Report the malaria status.
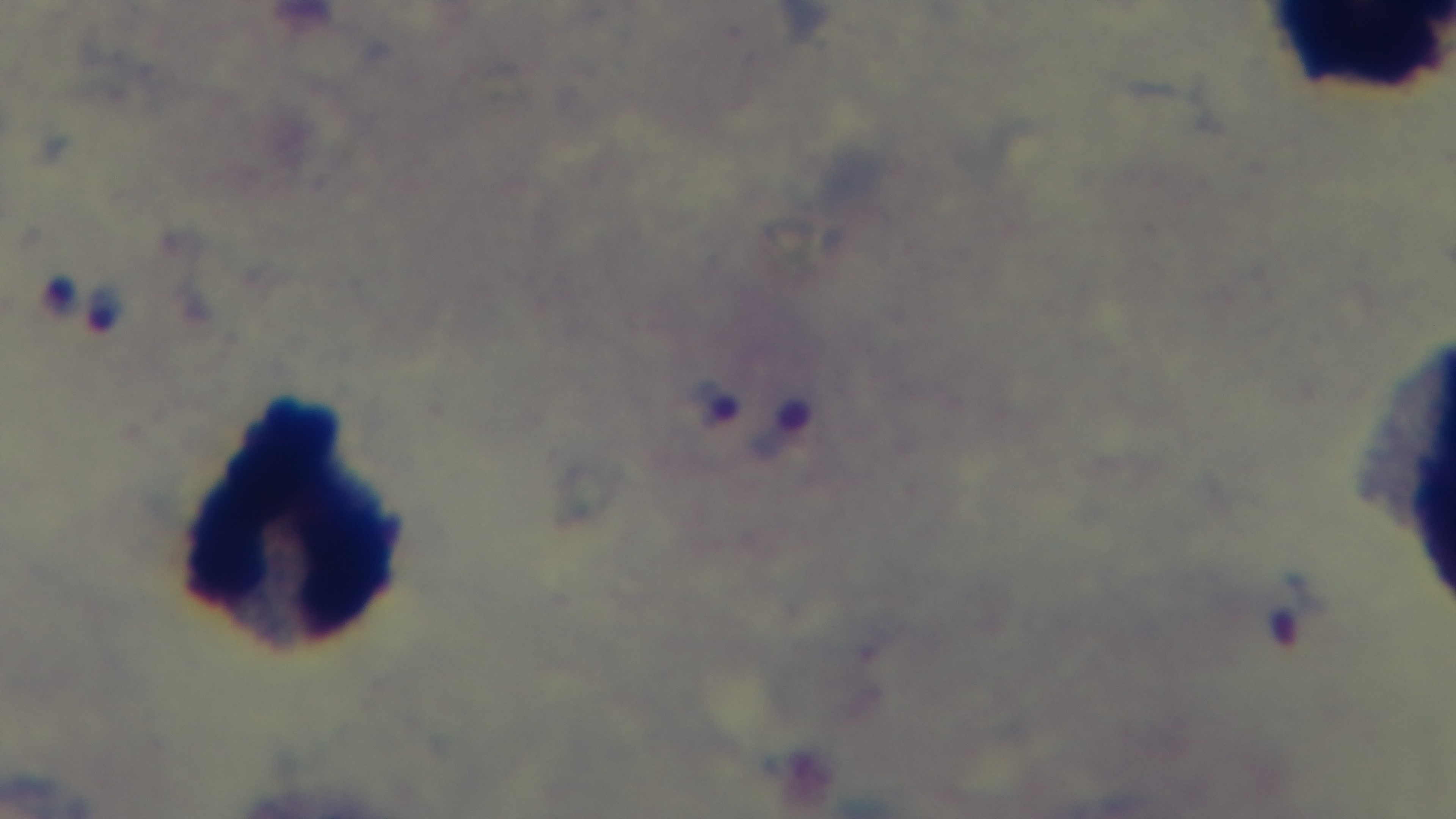
It is infected.

Summary:
  - Capture: mounted 4K digital camera
  - Preparation: thick blood film
  - Modality: light microscopy
  - Field of view: single
  - Stain: Giemsa
  - Objective: 100x oil immersion